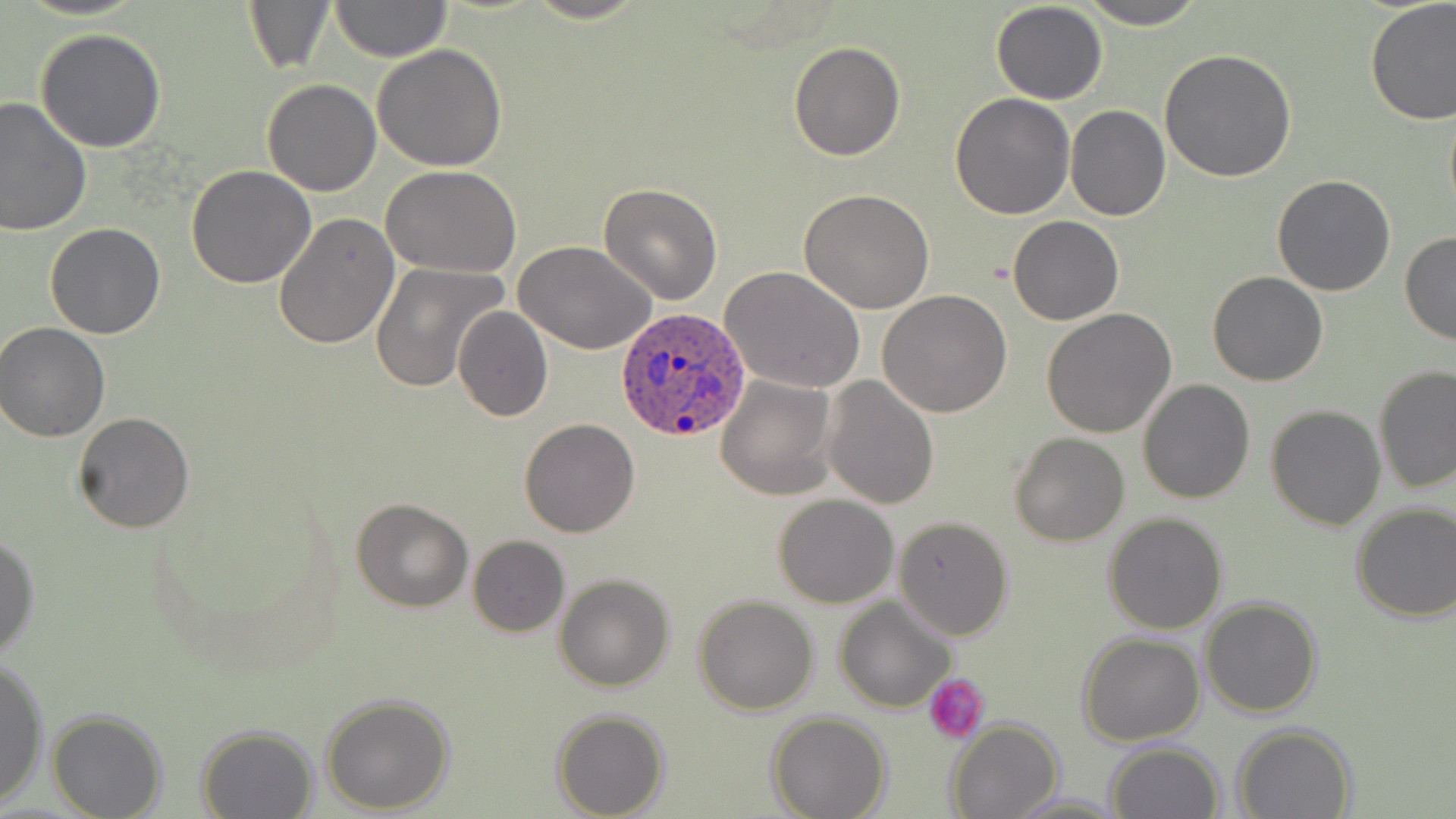

slide-level diagnosis = Plasmodium ovale
uninfected red blood cell locations = approximate bounding boxes as (x1, y1, x2, y2) in pixels: (244, 0, 335, 75), (522, 0, 650, 25), (1075, 0, 1207, 29), (1364, 0, 1455, 126), (329, 1, 453, 63), (991, 2, 1108, 104), (34, 28, 168, 153), (788, 41, 905, 161), (373, 44, 508, 171), (1159, 47, 1296, 182), (262, 79, 381, 197), (950, 94, 1075, 219), (0, 96, 93, 235), (1065, 105, 1169, 220), (185, 165, 316, 288), (382, 166, 520, 277), (1271, 174, 1398, 296), (598, 181, 722, 304), (799, 189, 935, 314), (273, 212, 400, 351), (1009, 216, 1124, 324), (44, 221, 166, 339), (1399, 231, 1456, 346), (515, 240, 658, 356), (370, 262, 509, 395), (721, 266, 868, 394), (1207, 270, 1328, 386), (876, 290, 1012, 417), (453, 306, 553, 423), (1041, 309, 1177, 437), (1, 322, 112, 440), (1373, 365, 1456, 496), (714, 374, 839, 500), (824, 375, 939, 509), (1137, 378, 1255, 504), (1265, 404, 1385, 531), (72, 412, 195, 532), (518, 420, 639, 538), (1009, 432, 1129, 546), (772, 495, 898, 608), (351, 496, 474, 612), (1350, 502, 1456, 622), (1102, 512, 1228, 634), (893, 516, 1014, 639), (0, 534, 39, 659), (467, 536, 570, 638), (554, 573, 675, 692), (694, 596, 819, 716), (836, 597, 957, 713), (1199, 598, 1323, 718), (1078, 633, 1203, 748), (0, 656, 49, 807), (319, 692, 454, 814), (551, 709, 670, 819), (47, 710, 167, 818), (767, 713, 891, 819), (946, 719, 1064, 819), (1231, 723, 1357, 819), (195, 724, 319, 818), (1105, 741, 1225, 819), (1006, 792, 1128, 817)
preparation = thin blood film
platelet locations = approximate bounding boxes as (x1, y1, x2, y2) in pixels: (924, 674, 991, 742)
field of view = one of a larger specimen
modality = optical microscopy
magnification = 1000x
Plasmodium ovale-infected red blood cell locations = approximate bounding boxes as (x1, y1, x2, y2) in pixels: (613, 308, 754, 444)
stain = May-Grünwald-Giemsa
image size = 1456×819 pixels